Describe the morphology of the erythrocytes.
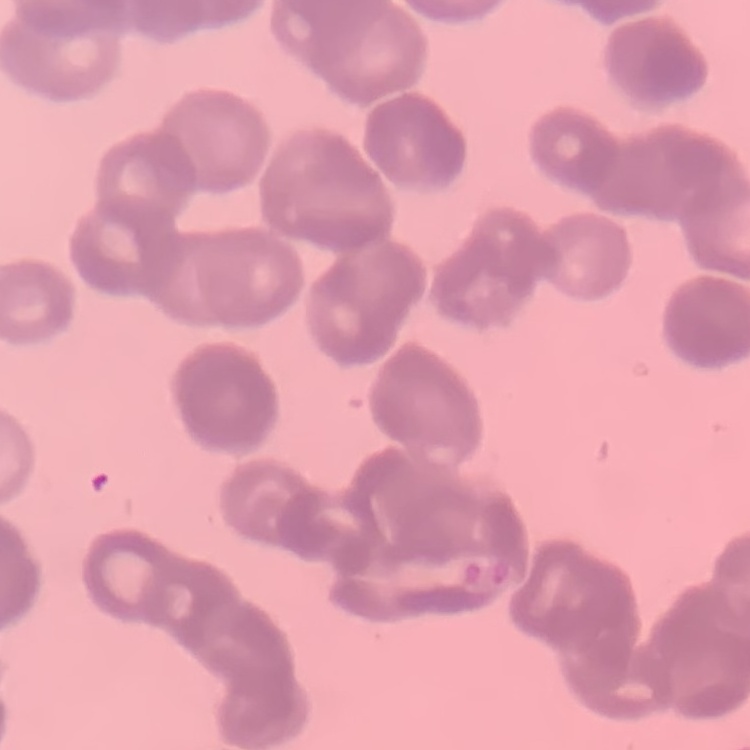

Rouleaux formation.

image_type: square crop of a larger photomicrograph
stain: Field's or Giemsa
preparation: thin blood film